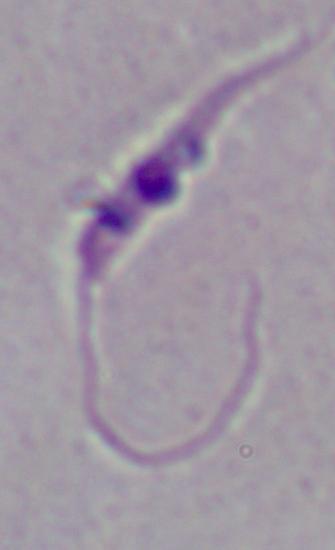
Captured at 1000x magnification. Photomicrograph. A Leishmania parasite is shown.